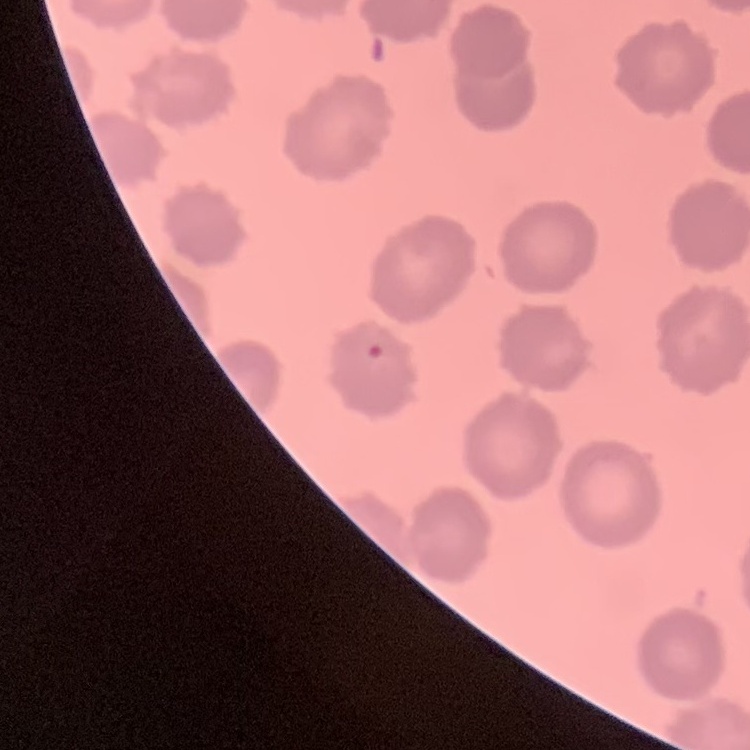

Summary:
  - Erythrocyte morphology: no rouleaux formation
  - Preparation: thin blood smear
  - Stain: Field's or Giemsa
  - Image type: square crop of a larger photomicrograph